Classify this cell by malaria status.
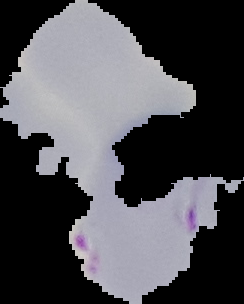

It is parasitized.

Summary:
  - Image type: segmented cell region on a black background
  - Image size: 244×304 pixels
  - Preparation: thin blood film